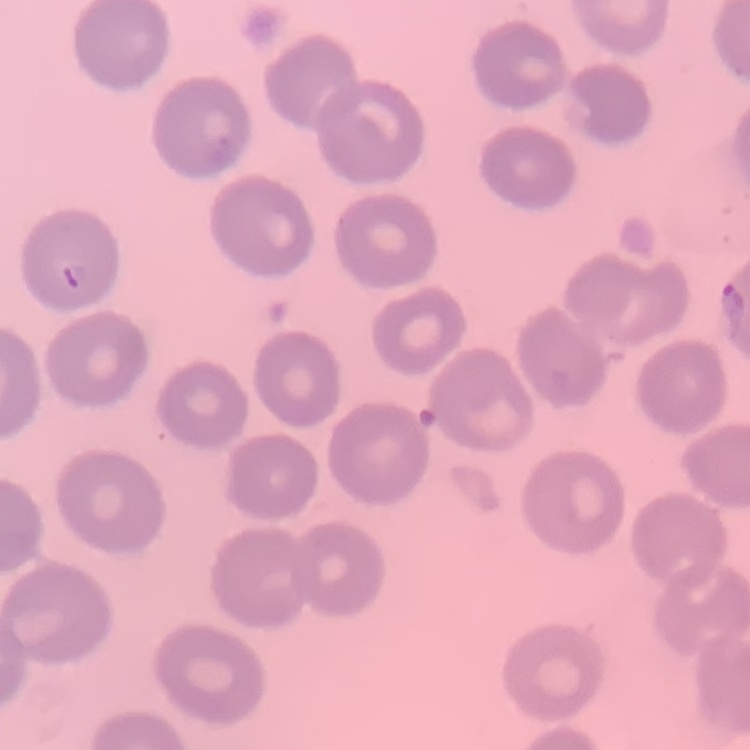

The erythrocytes exhibit no rouleaux formation. Stained with either Field's or Giemsa. Thin blood film. Square crop of a larger photomicrograph.